Classify this cell by malaria status.
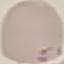
Uninfected.

stain: Giemsa
preparation: thin smear
image_type: automatically extracted cell patch, resized to 64 × 64 pixels
capture: smartphone through the microscope eyepiece